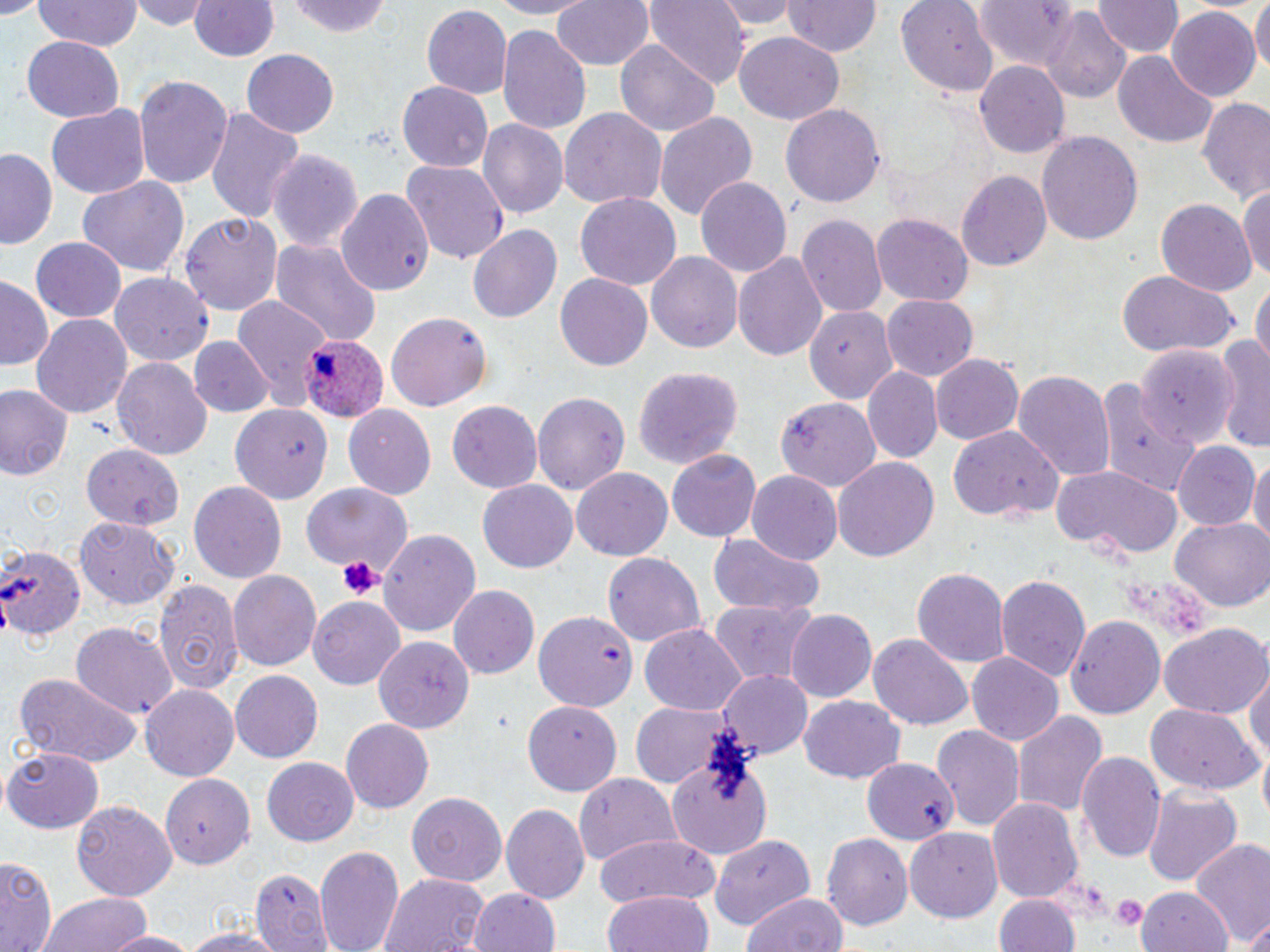

Approximate bounding boxes as [x1, y1, x2, y2] in pixels. Platelet locations: [337, 554, 384, 601], [1111, 894, 1147, 931]. Plasmodium ovale-infected red blood cell locations: [300, 333, 388, 423]. Uninfected red blood cell locations: [135, 0, 209, 31], [487, 0, 603, 18], [549, 0, 656, 74], [643, 0, 751, 87], [714, 0, 799, 32], [897, 0, 997, 91], [1091, 0, 1181, 58], [1251, 0, 1269, 81], [33, 1, 146, 52], [191, 1, 279, 62], [289, 1, 394, 39], [784, 1, 880, 58], [973, 1, 1086, 73], [420, 5, 513, 100], [1166, 7, 1260, 103], [1043, 11, 1133, 106], [496, 25, 592, 133], [733, 28, 842, 124], [22, 33, 124, 120], [613, 39, 719, 136], [242, 49, 339, 139], [1114, 52, 1218, 148], [975, 60, 1071, 158], [134, 75, 234, 192], [397, 81, 493, 172], [1196, 99, 1270, 204], [46, 104, 151, 201], [204, 104, 305, 222], [782, 104, 883, 209], [560, 108, 667, 209], [655, 112, 757, 227], [479, 118, 568, 219], [1037, 132, 1143, 246], [1, 146, 59, 250], [269, 149, 364, 254], [402, 160, 509, 265], [957, 169, 1053, 271], [77, 173, 191, 279], [695, 176, 792, 276], [1240, 182, 1270, 281], [335, 187, 434, 296], [575, 193, 682, 288], [1152, 198, 1257, 298], [181, 213, 281, 318], [800, 213, 887, 318], [872, 213, 973, 306], [468, 224, 561, 324], [30, 237, 128, 322], [272, 237, 380, 351], [646, 251, 743, 353], [733, 252, 828, 361], [1115, 268, 1235, 358], [110, 272, 214, 365], [554, 272, 654, 370], [0, 277, 52, 368], [1252, 280, 1269, 370], [231, 295, 331, 405], [882, 295, 979, 384], [807, 306, 898, 405], [385, 313, 492, 413], [31, 314, 131, 420], [1214, 334, 1270, 452], [189, 336, 274, 417], [1138, 340, 1238, 456], [930, 353, 1023, 446], [113, 357, 213, 461], [633, 367, 743, 469], [862, 367, 942, 463], [1013, 368, 1115, 481], [1092, 379, 1198, 497], [0, 384, 71, 482], [532, 388, 630, 492], [777, 395, 882, 490], [447, 399, 544, 493], [343, 403, 437, 499], [232, 406, 332, 503], [947, 427, 1064, 524], [80, 443, 184, 530], [1174, 443, 1257, 532], [667, 450, 761, 542], [1251, 456, 1270, 557], [832, 457, 940, 562], [1052, 464, 1182, 559], [572, 469, 672, 561], [748, 470, 842, 567], [478, 479, 577, 573], [189, 481, 288, 585], [303, 483, 408, 570], [1171, 517, 1270, 612], [77, 519, 180, 607], [377, 528, 481, 640], [708, 533, 826, 617], [0, 543, 82, 643], [602, 553, 707, 646], [913, 567, 1009, 669], [228, 569, 321, 673], [993, 572, 1092, 683], [153, 576, 243, 694], [449, 584, 539, 679], [309, 597, 405, 691], [708, 598, 820, 684], [535, 609, 638, 712], [785, 610, 877, 704], [1065, 615, 1166, 718], [70, 621, 177, 718], [1159, 622, 1268, 720], [640, 623, 747, 715], [868, 634, 972, 728], [375, 636, 471, 732], [965, 651, 1064, 746], [1244, 661, 1270, 775], [718, 669, 813, 757], [230, 670, 323, 761], [13, 672, 143, 767], [142, 684, 241, 781], [799, 697, 906, 784], [521, 699, 622, 797], [628, 703, 740, 789], [1145, 704, 1262, 795], [1011, 708, 1106, 820], [341, 718, 434, 812], [932, 724, 1025, 834], [3, 746, 103, 833], [1076, 749, 1167, 866], [670, 751, 772, 859], [861, 759, 960, 845], [264, 760, 358, 845], [163, 771, 256, 870], [573, 773, 680, 866], [1142, 787, 1240, 886], [406, 791, 507, 885], [990, 797, 1085, 906], [71, 800, 176, 901], [502, 805, 590, 905], [905, 829, 1001, 921], [821, 831, 911, 930], [709, 832, 816, 931], [594, 834, 721, 908], [1190, 839, 1270, 950], [314, 843, 404, 952], [1, 857, 56, 952], [250, 868, 332, 952], [377, 872, 490, 952], [1135, 887, 1233, 952], [468, 888, 563, 952], [602, 890, 712, 952], [33, 891, 156, 952], [990, 891, 1082, 952], [741, 892, 847, 952], [1243, 919, 1270, 952], [174, 928, 290, 952], [101, 930, 203, 952]. Slide-level diagnosis: Plasmodium ovale. May-Grünwald-Giemsa stain. Single field of view. Light microscopy. Image is 1270×952 pixels. Captured at 1000x magnification. Thin blood film.